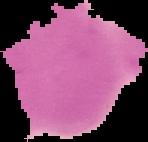 Image is 148×142 pixels. Malaria status: uninfected. The area outside the segmented cell region is set to black. From a thin blood film.